Name the blood parasite species.
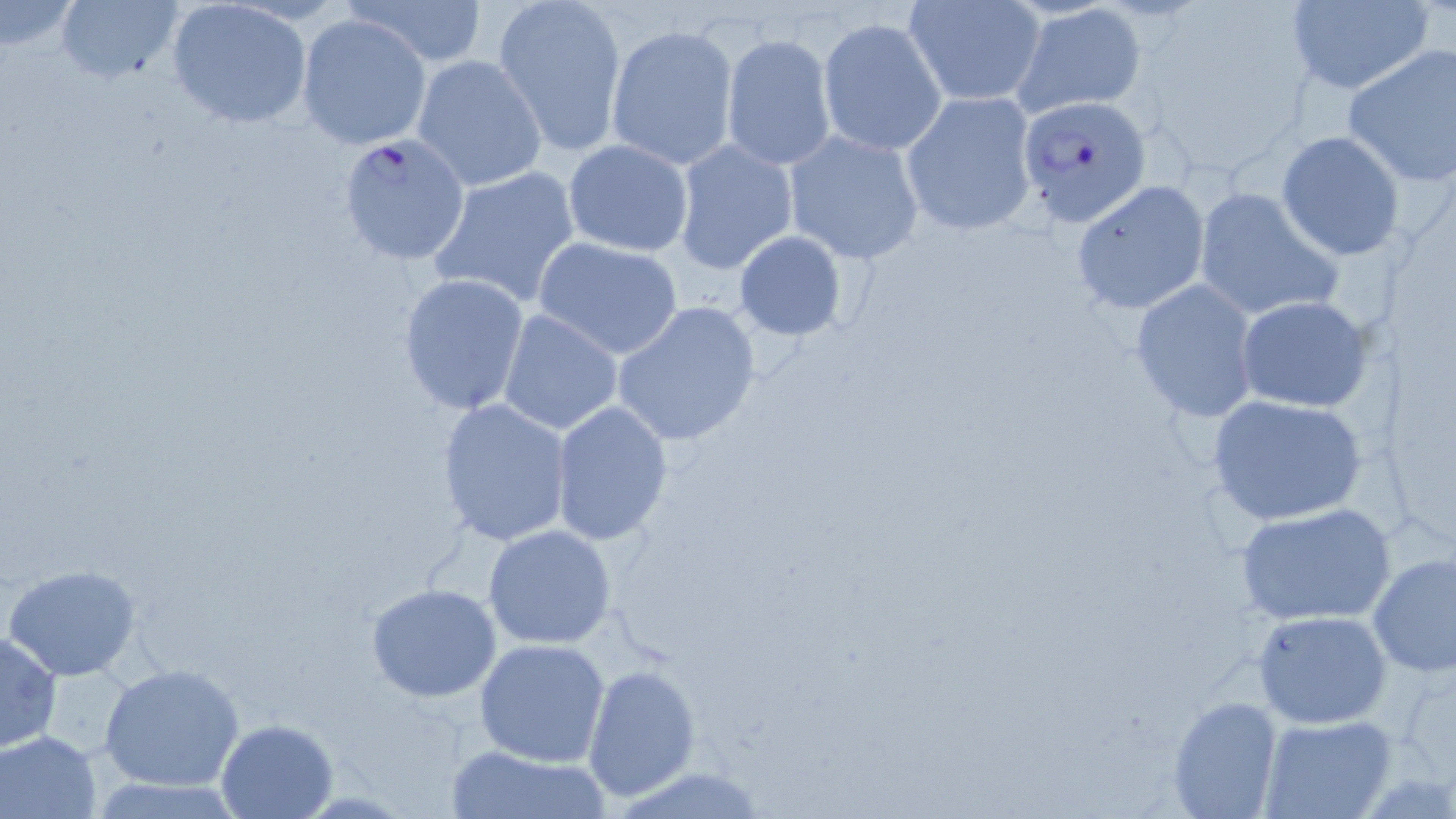

Plasmodium falciparum.

field of view = one of a larger specimen
magnification = 1000x
uninfected red blood cell locations = approximate bounding boxes as (x1, y1, x2, y2) in pixels: (0, 0, 81, 55), (55, 0, 184, 85), (350, 0, 490, 66), (494, 0, 627, 156), (904, 0, 1045, 107), (1284, 0, 1435, 94), (165, 2, 311, 129), (1011, 4, 1147, 115), (295, 14, 429, 149), (817, 17, 947, 157), (605, 22, 739, 170), (721, 34, 836, 170), (1343, 43, 1456, 186), (411, 54, 547, 191), (901, 91, 1039, 236), (784, 129, 926, 265), (1277, 131, 1403, 259), (670, 137, 799, 275), (562, 140, 694, 257), (427, 165, 581, 309), (1070, 180, 1210, 314), (1191, 186, 1345, 323), (733, 230, 846, 341), (532, 235, 685, 360), (396, 272, 531, 416), (1128, 279, 1260, 423), (1236, 296, 1371, 410), (610, 301, 761, 448), (497, 308, 624, 436), (1207, 394, 1367, 525), (437, 398, 572, 547), (550, 400, 672, 545), (1235, 503, 1396, 626), (482, 524, 617, 649), (1369, 552, 1456, 676), (2, 564, 144, 681), (365, 583, 504, 703), (1252, 608, 1393, 729), (0, 630, 62, 752), (473, 638, 612, 767), (99, 663, 244, 792), (584, 664, 701, 803), (1166, 694, 1284, 819), (1261, 715, 1396, 819), (213, 718, 338, 817), (0, 729, 102, 818), (447, 744, 607, 819)
preparation = thin blood film
stain = May-Grünwald-Giemsa
image size = 1456×819 pixels
Plasmodium falciparum-infected red blood cell locations = approximate bounding boxes as (x1, y1, x2, y2) in pixels: (1017, 95, 1152, 228), (342, 130, 476, 263)
modality = optical microscopy